Locate every blood parasite and identify its species.
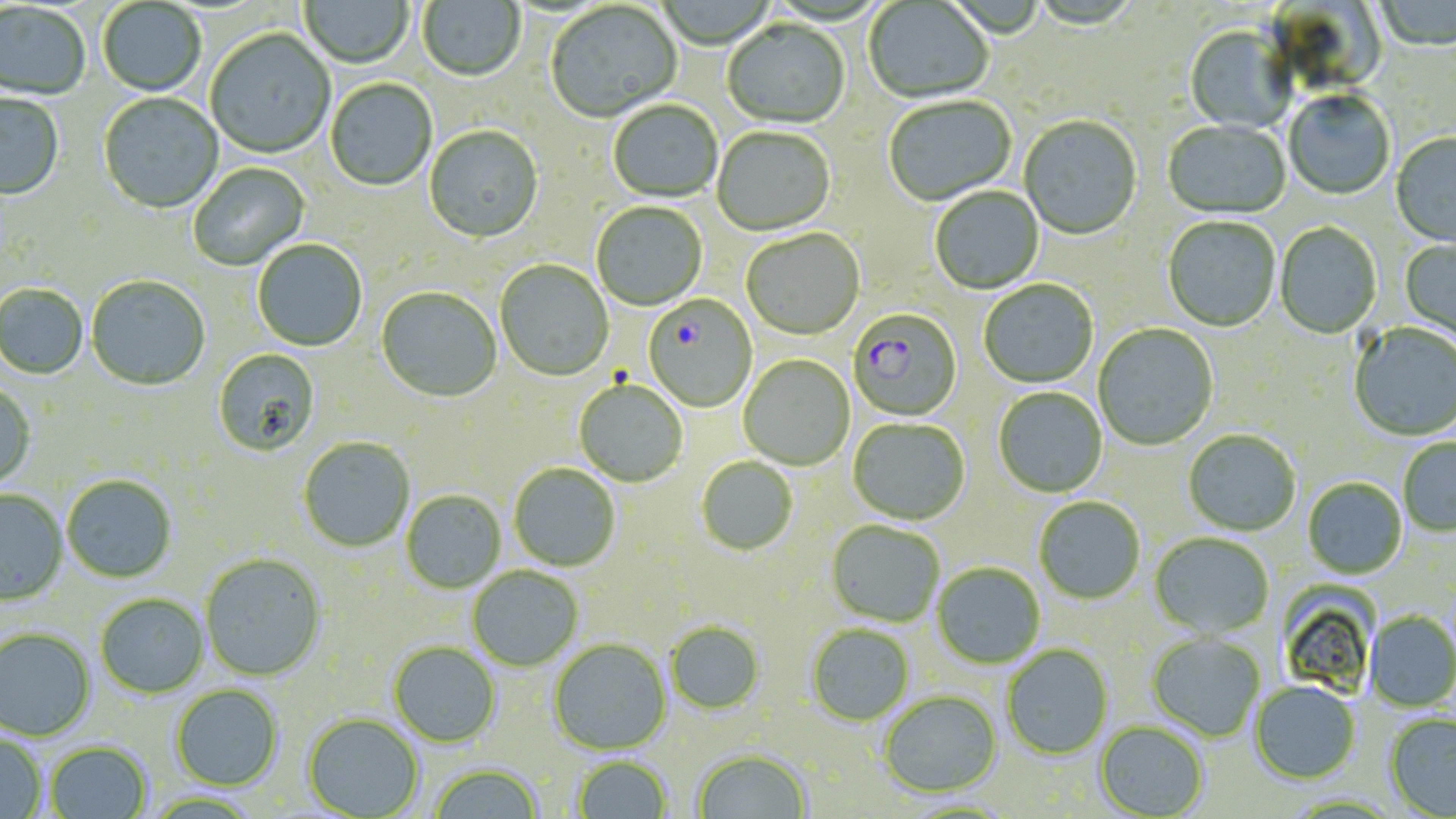
Approximate bounding boxes as [x1, y1, x2, y2] in pixels.
Plasmodium falciparum-infected red blood cells: [643, 296, 757, 413], [848, 309, 962, 422].
No Plasmodium ovale, Plasmodium malariae, Plasmodium vivax, Babesia divergens, or Trypanosoma brucei observed.

Summary:
  - Uninfected red blood cell locations: [300, 0, 413, 71], [418, 0, 525, 83], [864, 0, 993, 105], [98, 1, 206, 97], [1373, 1, 1455, 54], [1271, 2, 1385, 89], [0, 3, 90, 102], [546, 3, 682, 124], [722, 20, 850, 130], [1183, 25, 1296, 134], [205, 30, 335, 160], [325, 79, 437, 192], [1284, 92, 1394, 201], [98, 93, 224, 215], [0, 94, 64, 202], [884, 97, 1017, 207], [608, 101, 723, 204], [1019, 117, 1142, 241], [1163, 121, 1290, 221], [424, 127, 544, 245], [712, 128, 836, 237], [1391, 134, 1456, 247], [188, 164, 310, 272], [930, 187, 1044, 295], [591, 202, 707, 311], [1163, 217, 1280, 333], [1274, 223, 1382, 340], [741, 230, 865, 342], [1400, 238, 1456, 348], [252, 240, 367, 352], [495, 260, 614, 382], [86, 276, 210, 392], [979, 280, 1098, 388], [0, 285, 88, 381], [376, 288, 502, 403], [1349, 322, 1456, 443], [1093, 324, 1219, 451], [213, 349, 321, 457], [738, 355, 855, 471], [574, 381, 688, 488], [0, 385, 36, 490], [993, 387, 1107, 498], [848, 418, 970, 526], [1183, 430, 1301, 537], [298, 438, 415, 553], [1399, 438, 1456, 537], [696, 457, 798, 556], [509, 464, 620, 571], [62, 476, 177, 583], [1303, 478, 1407, 579], [0, 491, 68, 606], [401, 491, 506, 594], [1034, 496, 1145, 604], [826, 521, 945, 627], [1150, 532, 1274, 638], [200, 555, 326, 682], [932, 563, 1045, 670], [467, 567, 584, 673], [1278, 584, 1379, 698], [95, 594, 209, 699], [1365, 610, 1456, 712], [666, 621, 765, 715], [806, 624, 914, 726], [0, 628, 96, 742], [1147, 633, 1265, 742], [548, 639, 671, 755], [389, 642, 501, 748], [1001, 644, 1113, 760], [1250, 681, 1360, 784], [170, 684, 284, 791], [879, 690, 1002, 797], [303, 713, 424, 818], [1384, 713, 1456, 817], [1095, 721, 1209, 818], [0, 732, 47, 819], [45, 741, 152, 819], [692, 748, 812, 818], [571, 755, 673, 818], [427, 762, 545, 818]
  - Slide-level diagnosis: Plasmodium falciparum
  - Preparation: thin blood film
  - Modality: optical microscopy
  - Field of view: one of a larger specimen
  - Magnification: 1000x
  - Stain: May-Grünwald-Giemsa
  - Image size: 1456×819 pixels